Outline each Plasmodium falciparum-infected red blood cell.
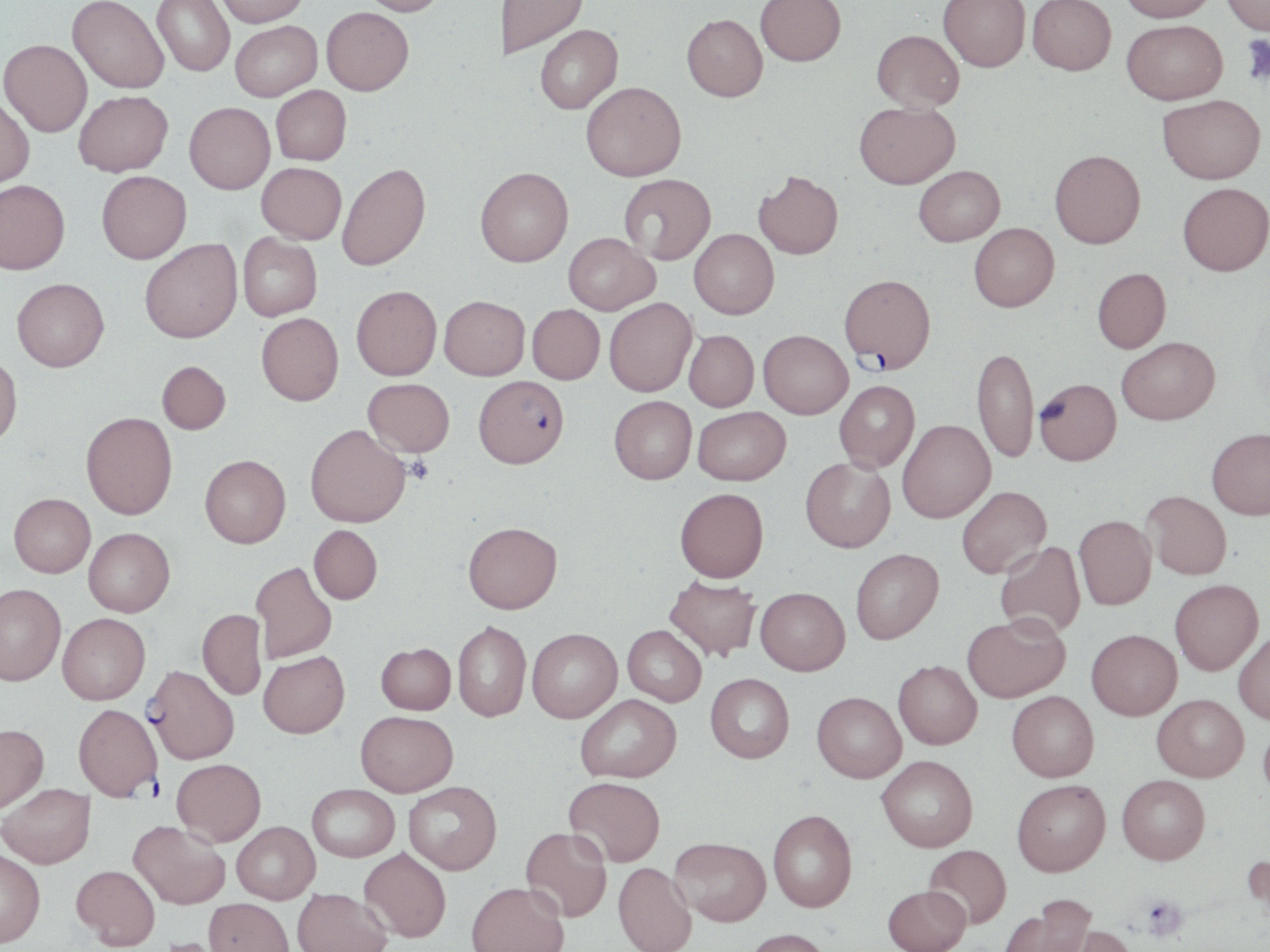

Approximate bounding boxes as [x1, y1, x2, y2] in pixels.
Plasmodium falciparum-infected red blood cells: [839, 274, 936, 370], [474, 375, 569, 467], [144, 664, 239, 764], [73, 704, 162, 799].

Uninfected red blood cell locations: [67, 0, 169, 93], [152, 0, 235, 76], [215, 0, 308, 27], [359, 0, 450, 16], [502, 0, 587, 57], [756, 0, 846, 65], [939, 0, 1030, 72], [1028, 0, 1116, 75], [1119, 0, 1217, 22], [1222, 0, 1269, 35], [321, 7, 413, 95], [681, 14, 768, 101], [1122, 19, 1227, 104], [230, 21, 322, 101], [535, 25, 623, 114], [872, 29, 964, 112], [0, 39, 92, 137], [581, 81, 686, 181], [271, 85, 351, 165], [74, 90, 173, 176], [1158, 95, 1266, 184], [0, 96, 34, 189], [854, 101, 960, 188], [185, 102, 275, 194], [1049, 149, 1146, 247], [257, 162, 346, 244], [336, 162, 430, 270], [914, 165, 1004, 246], [475, 167, 573, 266], [754, 170, 843, 259], [97, 171, 191, 263], [619, 174, 716, 264], [0, 180, 70, 274], [1177, 182, 1270, 275], [969, 223, 1059, 311], [689, 229, 779, 319], [238, 232, 322, 321], [564, 232, 658, 315], [139, 239, 242, 343], [1092, 267, 1171, 353], [12, 278, 109, 371], [351, 285, 442, 380], [439, 295, 530, 380], [604, 297, 697, 396], [527, 304, 605, 383], [256, 312, 344, 405], [684, 330, 759, 411], [759, 330, 852, 418], [1116, 336, 1220, 424], [972, 346, 1039, 463], [0, 354, 22, 447], [157, 361, 231, 434], [363, 378, 454, 457], [1034, 378, 1122, 464], [834, 380, 920, 472], [609, 395, 697, 484], [693, 406, 791, 485], [81, 412, 177, 519], [897, 420, 995, 522], [305, 424, 411, 527], [1206, 427, 1270, 519], [200, 454, 290, 547], [800, 457, 895, 552], [956, 486, 1051, 578], [674, 487, 768, 582], [1142, 490, 1232, 579], [9, 493, 95, 577], [1074, 514, 1156, 610], [463, 522, 562, 613], [309, 525, 382, 604], [84, 527, 175, 616], [995, 541, 1086, 638], [851, 548, 944, 644], [252, 561, 337, 663], [664, 575, 761, 661], [1170, 579, 1263, 675], [0, 582, 66, 685], [755, 587, 850, 675], [197, 609, 267, 699], [58, 613, 150, 704], [963, 614, 1070, 702], [453, 621, 531, 721], [623, 625, 707, 706], [528, 628, 622, 722], [1086, 629, 1181, 720], [1233, 631, 1270, 724], [376, 643, 456, 714], [258, 650, 350, 738], [893, 660, 982, 749], [705, 673, 794, 762], [1006, 690, 1099, 781], [812, 692, 906, 782], [1152, 693, 1249, 781], [575, 694, 681, 782], [355, 710, 458, 796], [1258, 717, 1270, 805], [0, 724, 48, 813], [877, 755, 978, 851], [172, 758, 266, 845], [1117, 774, 1210, 864], [564, 776, 666, 866], [1012, 779, 1110, 876], [403, 781, 501, 874], [1, 783, 95, 868], [307, 784, 399, 861], [768, 809, 857, 912], [130, 820, 230, 909], [232, 821, 320, 903], [520, 827, 612, 922], [670, 836, 771, 925], [924, 844, 1011, 928], [0, 847, 45, 947], [359, 848, 451, 942], [1244, 848, 1270, 929], [613, 861, 697, 952], [72, 864, 160, 949], [467, 881, 569, 952], [883, 884, 970, 952], [292, 888, 392, 952], [204, 898, 294, 952], [1000, 898, 1097, 952], [1066, 925, 1139, 952], [743, 928, 833, 952]. Platelet locations: [1240, 35, 1270, 86], [405, 456, 433, 484], [1139, 894, 1188, 941]. Slide-level diagnosis: Plasmodium falciparum. Image is 1270×952 pixels. May-Grünwald-Giemsa stain. Light microscopy. Thin blood smear. Captured at 1000x magnification. Single field of view.